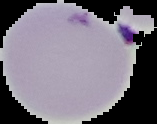
From a thin blood film. Segmented cell region on a black background. Image is 157×124 pixels. Result: malaria parasites detected.